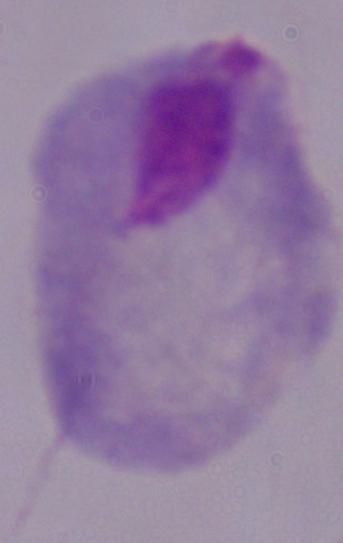
Summary:
  - Modality: micrograph
  - Identification: trichomonad
  - Magnification: 1000x